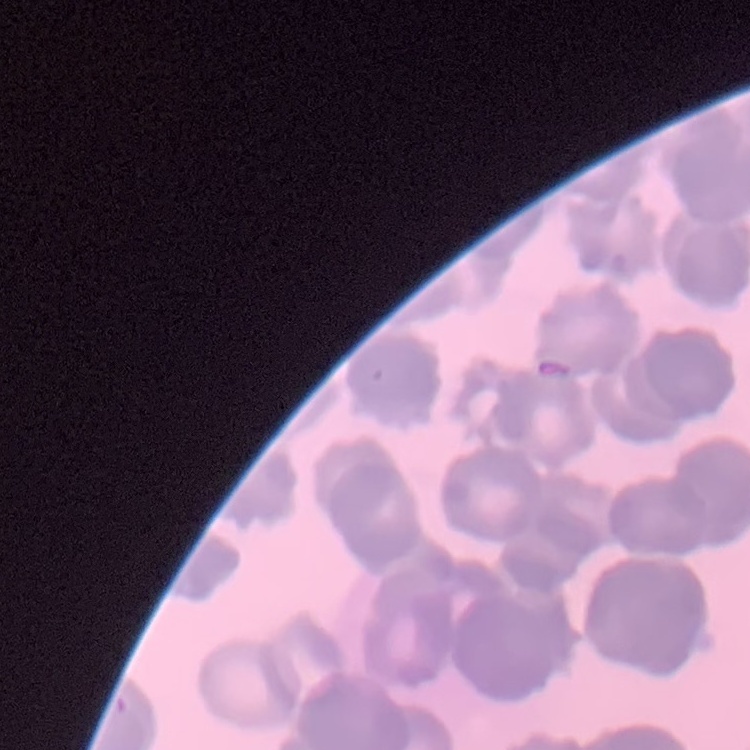

erythrocyte morphology = rouleaux formation
preparation = thin blood film
stain = Field's or Giemsa
image type = one tile cut from a larger photomicrograph